Identify the cell.
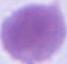

An erythrocyte.

Micrograph. 1000x magnification.